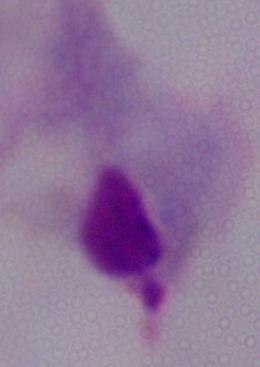

identification = trichomonad
modality = micrograph
magnification = 1000x